Locate every Plasmodium vivax-infected red blood cell.
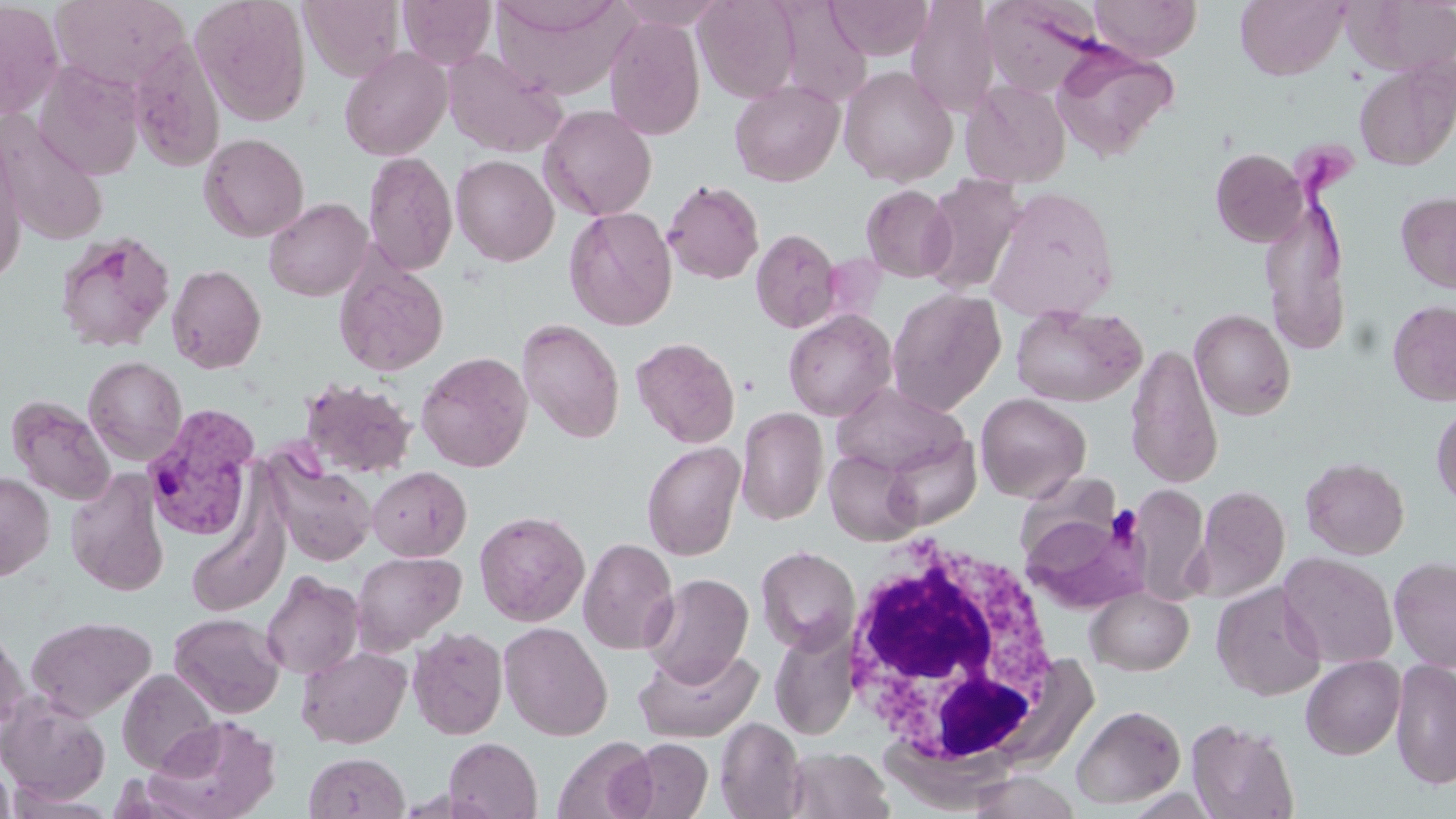

Approximate bounding boxes as (x1, y1, x2, y2) in pixels.
Plasmodium vivax-infected red blood cells: (141, 404, 260, 540).

{
  "slide_level_diagnosis": "Plasmodium vivax",
  "preparation": "thin blood smear",
  "image_size": "1456×819 pixels",
  "modality": "light microscopy",
  "stain": "May-Grünwald-Giemsa",
  "field_of_view": "one of a larger specimen",
  "magnification": "1000x",
  "white_blood_cell_locations": "approximate bounding boxes as (x1, y1, x2, y2) in pixels: (838, 536, 1070, 782)",
  "uninfected_red_blood_cell_locations": "approximate bounding boxes as (x1, y1, x2, y2) in pixels: (50, 0, 190, 91), (190, 0, 312, 126), (398, 0, 496, 69), (492, 0, 630, 100), (610, 0, 722, 30), (694, 0, 801, 102), (825, 0, 933, 60), (1089, 0, 1201, 62), (1235, 0, 1349, 79), (1344, 0, 1455, 78), (300, 1, 405, 82), (907, 1, 999, 117), (982, 1, 1102, 97), (0, 2, 64, 120), (604, 15, 706, 141), (127, 36, 225, 172), (1051, 41, 1179, 161), (339, 46, 452, 161), (441, 48, 567, 158), (1354, 54, 1456, 172), (33, 61, 145, 180), (839, 65, 958, 186), (961, 79, 1072, 188), (729, 80, 844, 186), (538, 104, 657, 220), (0, 117, 108, 246), (198, 132, 309, 242), (0, 142, 26, 286), (1211, 148, 1308, 246), (363, 151, 458, 275), (451, 154, 559, 266), (918, 172, 1028, 297), (662, 179, 764, 285), (861, 184, 956, 283), (985, 186, 1120, 322), (1396, 191, 1456, 294), (1259, 193, 1350, 354), (263, 198, 372, 301), (564, 206, 678, 330), (750, 228, 843, 333), (54, 230, 177, 353), (334, 257, 449, 377), (166, 264, 266, 373), (886, 288, 1006, 414), (1387, 300, 1456, 406), (1010, 304, 1146, 408), (1190, 308, 1296, 420), (783, 309, 897, 421), (517, 318, 624, 443), (630, 337, 740, 448), (1125, 343, 1223, 489), (416, 351, 534, 472), (83, 356, 187, 465), (298, 377, 418, 479), (831, 384, 967, 478), (975, 393, 1091, 502), (8, 396, 115, 505), (1431, 402, 1456, 509), (736, 407, 828, 525), (880, 430, 982, 531), (643, 441, 745, 560), (824, 448, 922, 545), (266, 454, 376, 566), (1301, 457, 1409, 559), (367, 466, 472, 561), (65, 468, 169, 597), (0, 471, 55, 581), (1128, 483, 1211, 604), (1192, 484, 1289, 602), (1021, 508, 1153, 614), (474, 510, 590, 626), (187, 517, 287, 617), (578, 537, 679, 655), (755, 545, 860, 654), (351, 550, 466, 654), (1278, 552, 1398, 668), (1389, 556, 1456, 672), (260, 571, 364, 679), (641, 572, 754, 687), (1211, 582, 1327, 701), (1085, 586, 1194, 675), (169, 612, 285, 718), (26, 615, 156, 720), (498, 621, 613, 741), (0, 624, 29, 736), (407, 626, 508, 739), (768, 627, 859, 740), (296, 645, 412, 748), (634, 645, 763, 742), (1301, 655, 1405, 759), (1391, 657, 1456, 790), (117, 668, 219, 775), (0, 692, 111, 806), (1071, 704, 1186, 809), (146, 715, 282, 819), (715, 717, 807, 818), (1186, 717, 1299, 819), (552, 735, 657, 819), (444, 737, 542, 819), (617, 737, 713, 819), (784, 747, 893, 819), (303, 752, 409, 819), (0, 757, 17, 819), (965, 771, 1082, 818)",
  "platelet_locations": "approximate bounding boxes as (x1, y1, x2, y2) in pixels: (1109, 507, 1144, 545)"
}